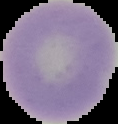

Summary:
  - Image type: cell region segmented out of the field of view; surrounding area masked to black
  - Preparation: thin blood smear
  - Image size: 118×124 pixels
  - Malaria status: uninfected